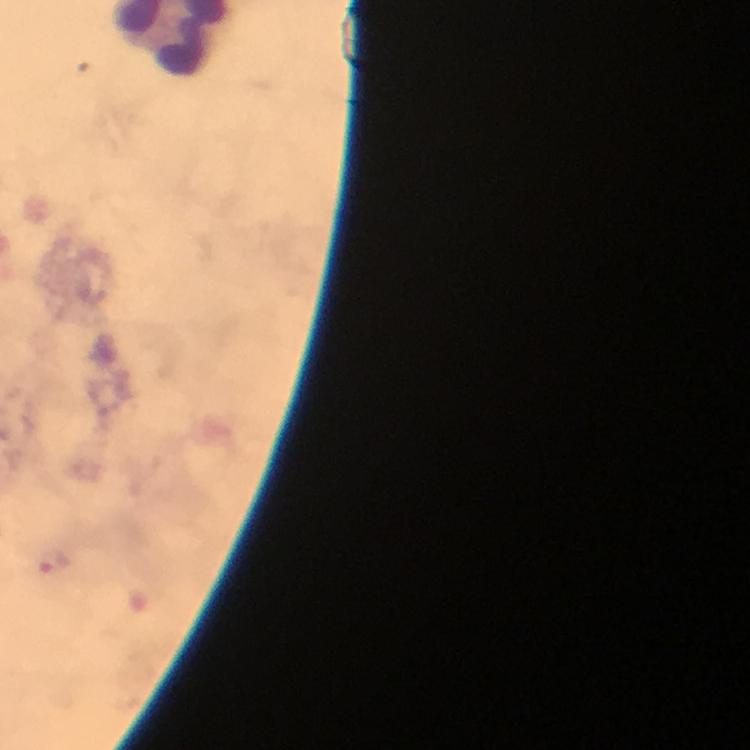

Approximate centers as [x, y] in pixels.
Summary:
  - Plasmodium parasite locations: [54, 559]
  - Stain: Giemsa
  - Preparation: thick blood film
  - Capture: smartphone photograph through a microscope
  - Image size: 750×750 pixels
  - Magnification: 100x
  - Immersion oil: used
  - Context: from a malaria diagnostic workup
  - Cropped from: one field of view